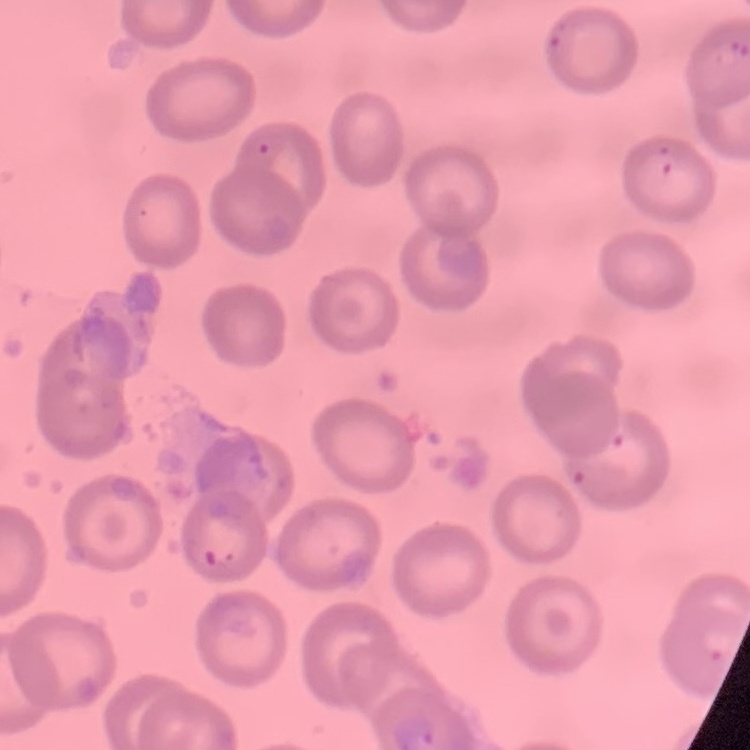
Summary:
  - Red blood cell morphology: no rouleaux formation
  - Stain: Field's or Giemsa
  - Image type: one tile cut from a larger photomicrograph
  - Preparation: thin blood smear